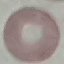

Malaria status: uninfected. Automatically extracted cell patch, resized to 64 × 64 pixels. Photographed with a smartphone camera at the microscope eyepiece. Thin blood smear. Giemsa-stained preparation.